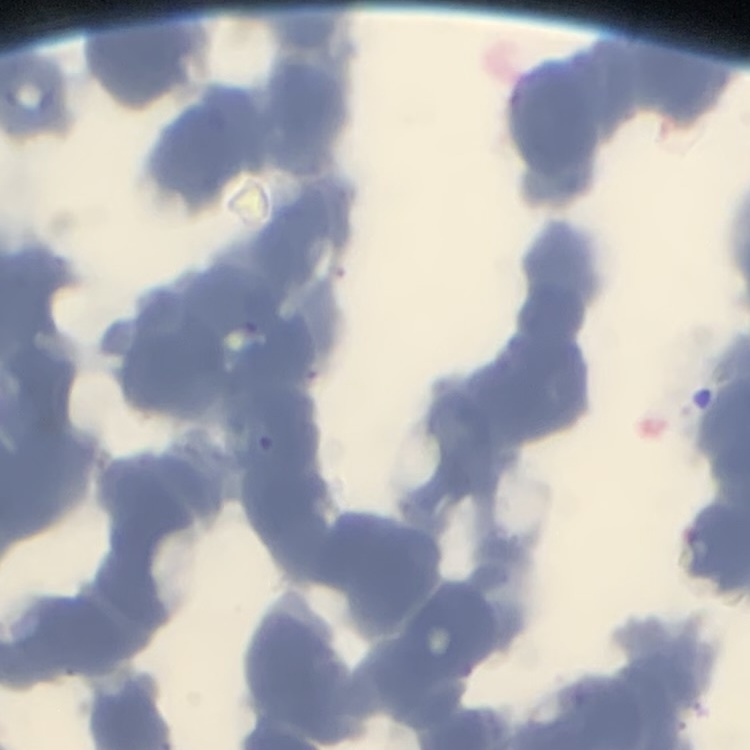

The erythrocytes exhibit rouleaux formation. Thin blood smear. One tile cut from a larger photomicrograph. Stained with either Field's or Giemsa.